Assess the morphology of the erythrocytes.
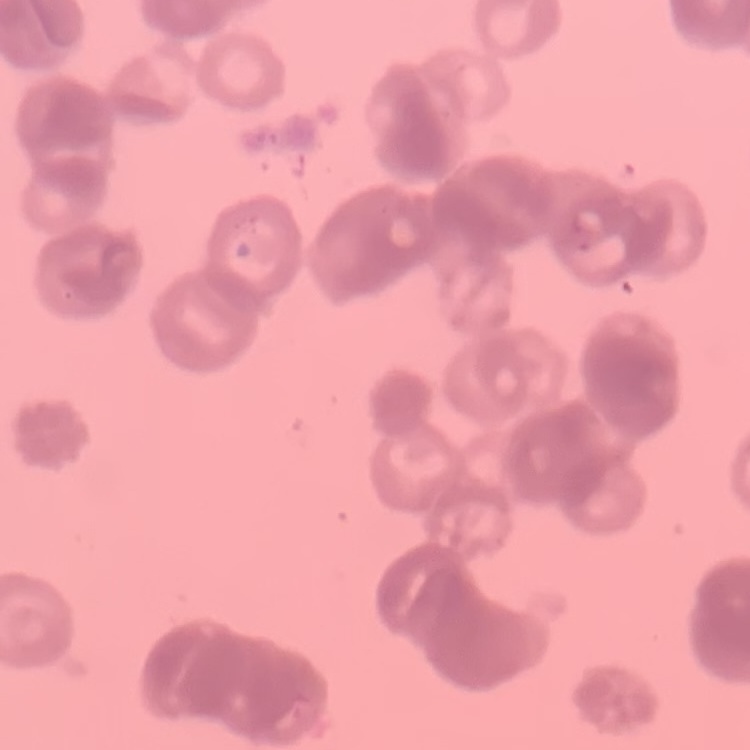
Rouleaux formation.

image type = one tile cut from a larger photomicrograph
preparation = thin blood film
stain = Field's or Giemsa